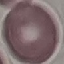 Malaria status: uninfected. Automatically extracted cell patch, resized to 64 × 64 pixels. Thin blood smear. Photographed with a smartphone camera at the microscope eyepiece. Giemsa stain.